Classify this cell by malaria status.
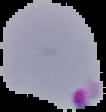
It is parasitized.

Image is 106×112 pixels. Segmented cell region on a black background. From a thin blood film.